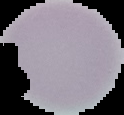
preparation = thin blood smear
image type = segmented cell region on a black background
result = no Plasmodium parasites detected
image size = 124×115 pixels